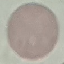
malaria status = uninfected
image type = automatically extracted cell patch, resized to 64 × 64 pixels
capture = smartphone camera at the microscope eyepiece
preparation = thin smear
stain = Giemsa